Identify the parasite.
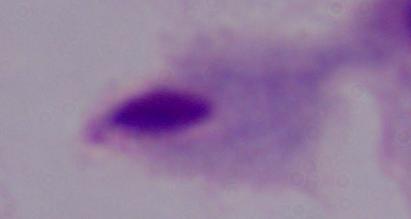
This is a trichomonad.

magnification = 1000x
modality = micrograph